Classify this cell by malaria status.
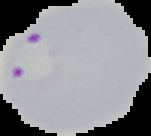

Parasitized.

Image is 151×136 pixels. From a thin blood film. Segmented cell region on a black background.